Report the malaria status of this cell.
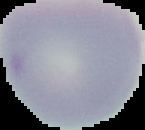
Uninfected.

From a thin blood film. Image is 145×130 pixels. The area outside the segmented cell region is set to black.